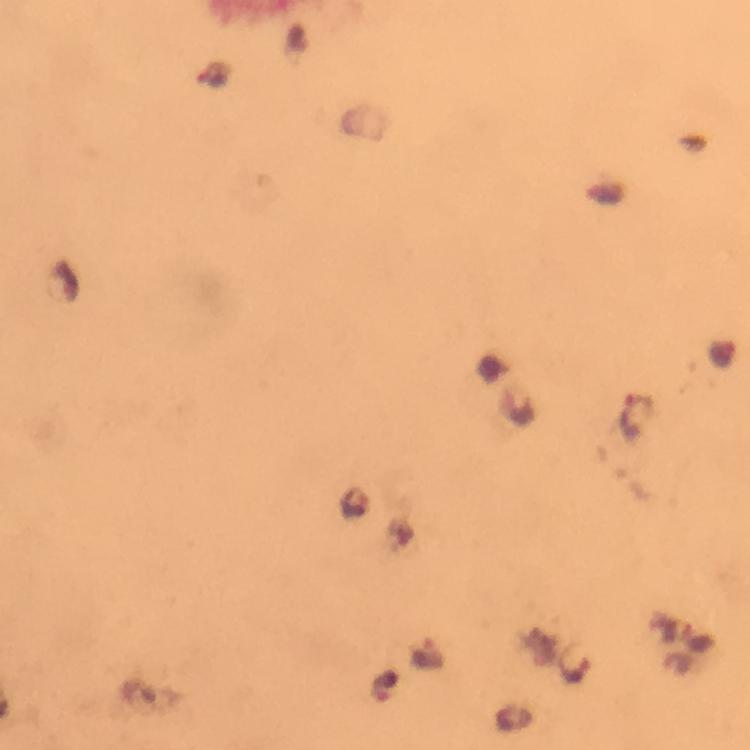

Approximate object centers, in pixels from the top-left corner. Malaria parasite locations: (x=722, y=353), (x=633, y=416), (x=700, y=639), (x=430, y=653), (x=578, y=667), (x=384, y=686). Immersion oil was used. 100x magnification. Giemsa-stained preparation. Thick blood smear. Photographed through the microscope with a smartphone camera. From a diagnostic examination for malaria. Cropped region of a single field of view. Image is 750×750 pixels.